Locate every uninfected red blood cell.
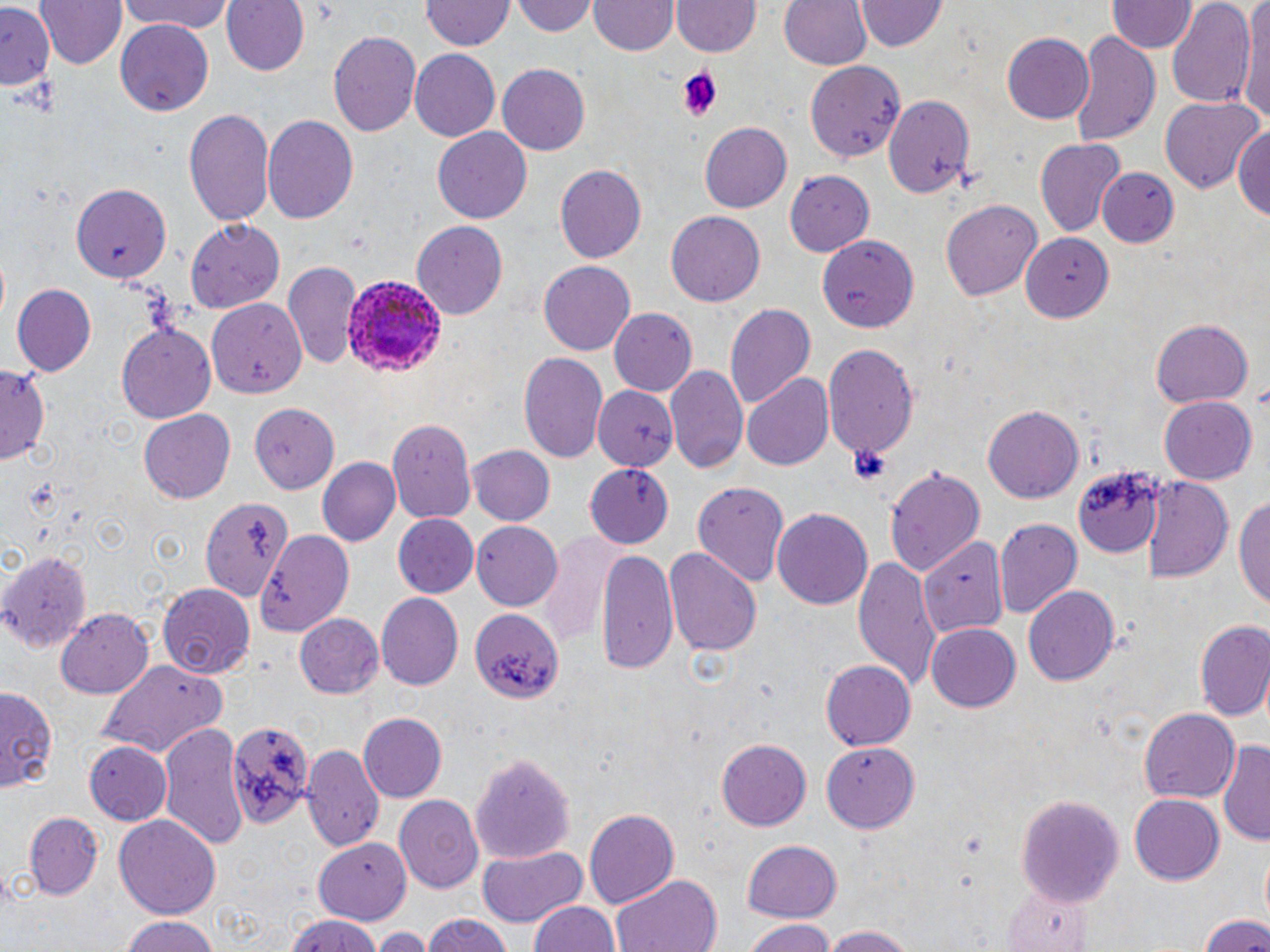
Approximate bounding boxes as (x1,y1)-(x2,y2) corner pairs in pixels.
Uninfected red blood cells: (38,0)-(126,69), (121,0)-(232,35), (220,0)-(307,77), (515,0)-(598,37), (777,0)-(872,73), (1109,0)-(1194,54), (423,1)-(511,53), (589,1)-(675,57), (673,1)-(760,58), (856,1)-(946,53), (1167,1)-(1257,113), (1241,1)-(1270,126), (0,3)-(54,90), (115,19)-(216,115), (328,31)-(421,137), (1069,32)-(1159,146), (1002,33)-(1095,123), (408,48)-(499,142), (805,61)-(908,162), (498,63)-(591,156), (1160,96)-(1264,190), (884,97)-(973,200), (185,105)-(277,229), (261,113)-(360,227), (1231,119)-(1269,224), (701,120)-(793,214), (432,126)-(532,220), (1035,139)-(1125,237), (554,163)-(647,264), (1095,167)-(1178,249), (788,169)-(874,255), (73,184)-(172,281), (941,198)-(1042,304), (666,211)-(765,307), (185,218)-(285,309), (412,222)-(508,318), (820,233)-(917,329), (1020,236)-(1116,323), (285,260)-(362,370), (540,260)-(637,356), (11,284)-(98,377), (207,297)-(307,399), (725,302)-(816,412), (609,306)-(699,396), (1149,317)-(1253,408), (117,321)-(217,424), (822,344)-(917,464), (518,353)-(609,467), (665,363)-(750,477), (0,364)-(49,464), (740,375)-(834,473), (594,386)-(678,472), (1159,396)-(1257,485), (983,403)-(1084,505), (251,407)-(349,498), (137,411)-(236,504), (387,418)-(477,521), (468,445)-(556,527), (316,457)-(400,548), (584,463)-(674,548), (1071,463)-(1163,556), (884,464)-(986,579), (1142,473)-(1233,583), (691,478)-(788,585), (1236,489)-(1270,615), (202,495)-(296,607), (771,507)-(875,610), (392,514)-(479,599), (994,519)-(1082,620), (471,521)-(561,611), (257,527)-(355,634), (538,532)-(620,652), (919,540)-(1005,635), (665,544)-(762,657), (595,548)-(676,674), (0,550)-(92,651), (851,551)-(941,692), (1023,583)-(1120,684), (158,584)-(257,679), (375,593)-(464,692), (469,607)-(562,705), (57,609)-(153,699), (297,613)-(384,699), (1192,620)-(1269,722), (927,623)-(1020,712), (96,659)-(228,757), (820,661)-(915,750), (0,683)-(59,797), (1139,706)-(1241,802), (358,713)-(447,803), (224,717)-(313,831), (158,719)-(249,853), (715,739)-(812,832), (1218,740)-(1270,846), (86,741)-(171,825), (822,741)-(919,832), (301,745)-(384,853), (471,750)-(576,889), (393,794)-(483,892), (1017,795)-(1125,900), (1130,795)-(1223,884), (582,807)-(679,909), (21,811)-(106,902), (115,815)-(220,923), (313,837)-(413,923), (740,838)-(843,922), (477,845)-(586,924), (611,874)-(723,952), (528,900)-(623,952), (1195,913)-(1270,952), (420,914)-(516,952), (115,915)-(222,952), (282,917)-(386,952), (742,918)-(834,951), (814,924)-(920,952), (372,926)-(430,952).

slide-level diagnosis = Plasmodium ovale
field of view = one of a larger specimen
stain = May-Grünwald-Giemsa
Plasmodium ovale-infected red blood cell locations = approximate bounding boxes as (x1,y1)-(x2,y2) corner pairs in pixels: (344,273)-(448,378)
image size = 1270×952 pixels
modality = optical microscopy
magnification = 1000x
platelet locations = approximate bounding boxes as (x1,y1)-(x2,y2) corner pairs in pixels: (679,65)-(722,119), (846,444)-(893,485), (23,480)-(66,519)
preparation = thin blood film